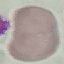

Result: no malaria parasites seen. Acquired by smartphone through the microscope eyepiece. Cell patch, automatically extracted from a larger field of view and resized to 64 × 64 pixels. Giemsa-stained preparation. Thin blood smear.